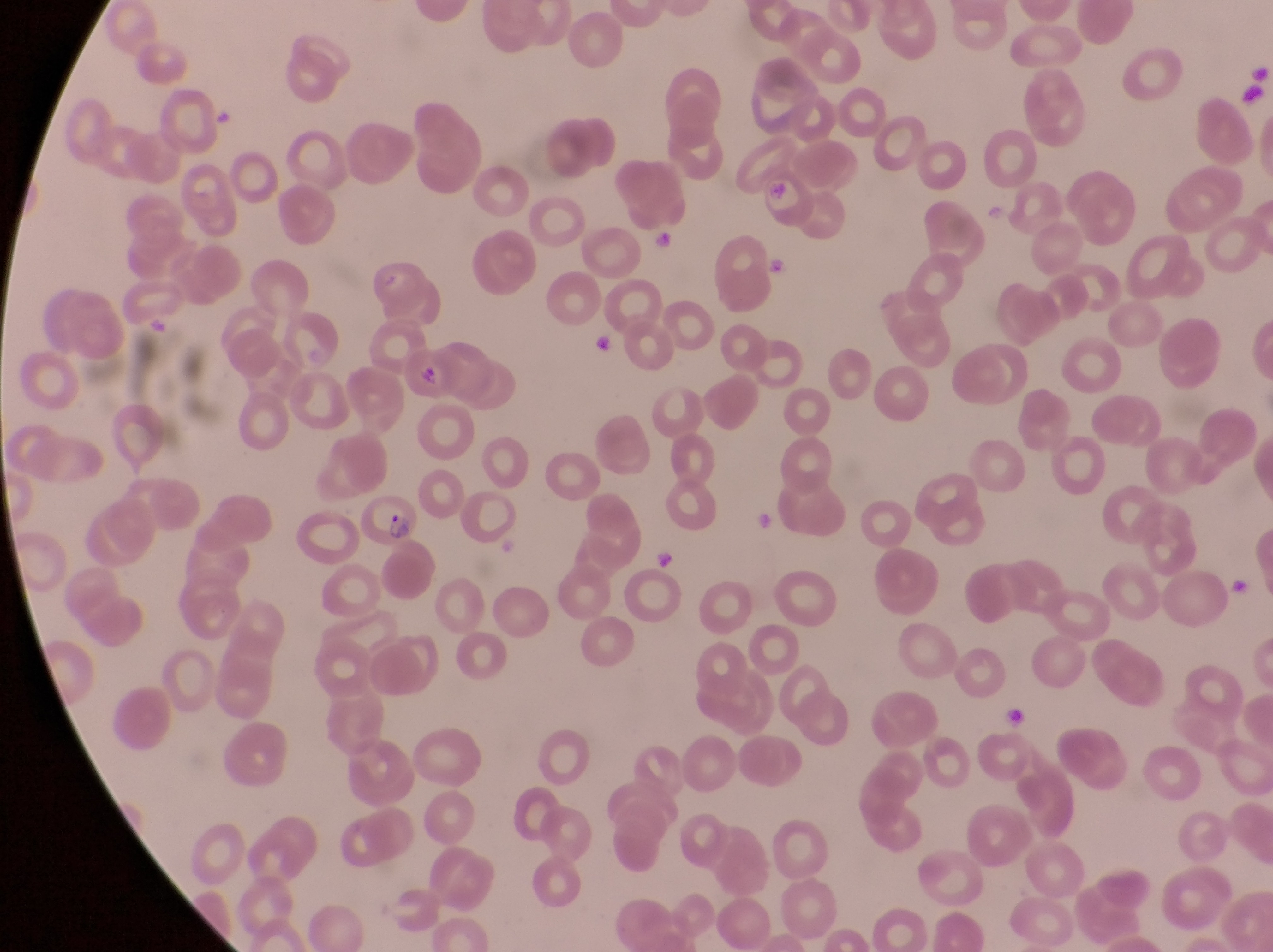
Approximate bounding boxes as (left, top, right, bottom) in pixels.
Summary:
  - Parasitised red blood cell locations: (759, 170, 817, 225), (402, 354, 450, 402), (359, 492, 422, 552)
  - Artifact (platelet-like body, stain precipitate, or debris) locations: (654, 233, 680, 253), (595, 332, 619, 356), (651, 543, 685, 572), (1003, 700, 1036, 728)
  - Field of view: single
  - Image size: 1273×952 pixels
  - Magnification: 1000x
  - Preparation: thin blood smear
  - Country: Uganda
  - Capture: smartphone photograph through the eyepiece of an Olympus CX-23 microscope